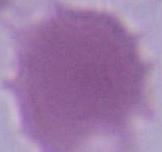
{
  "identification": "red blood cell",
  "magnification": "1000x",
  "modality": "photomicrograph"
}